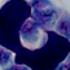 Captured at 1000x magnification. Photomicrograph. A leukocyte is shown.